Report the malaria status.
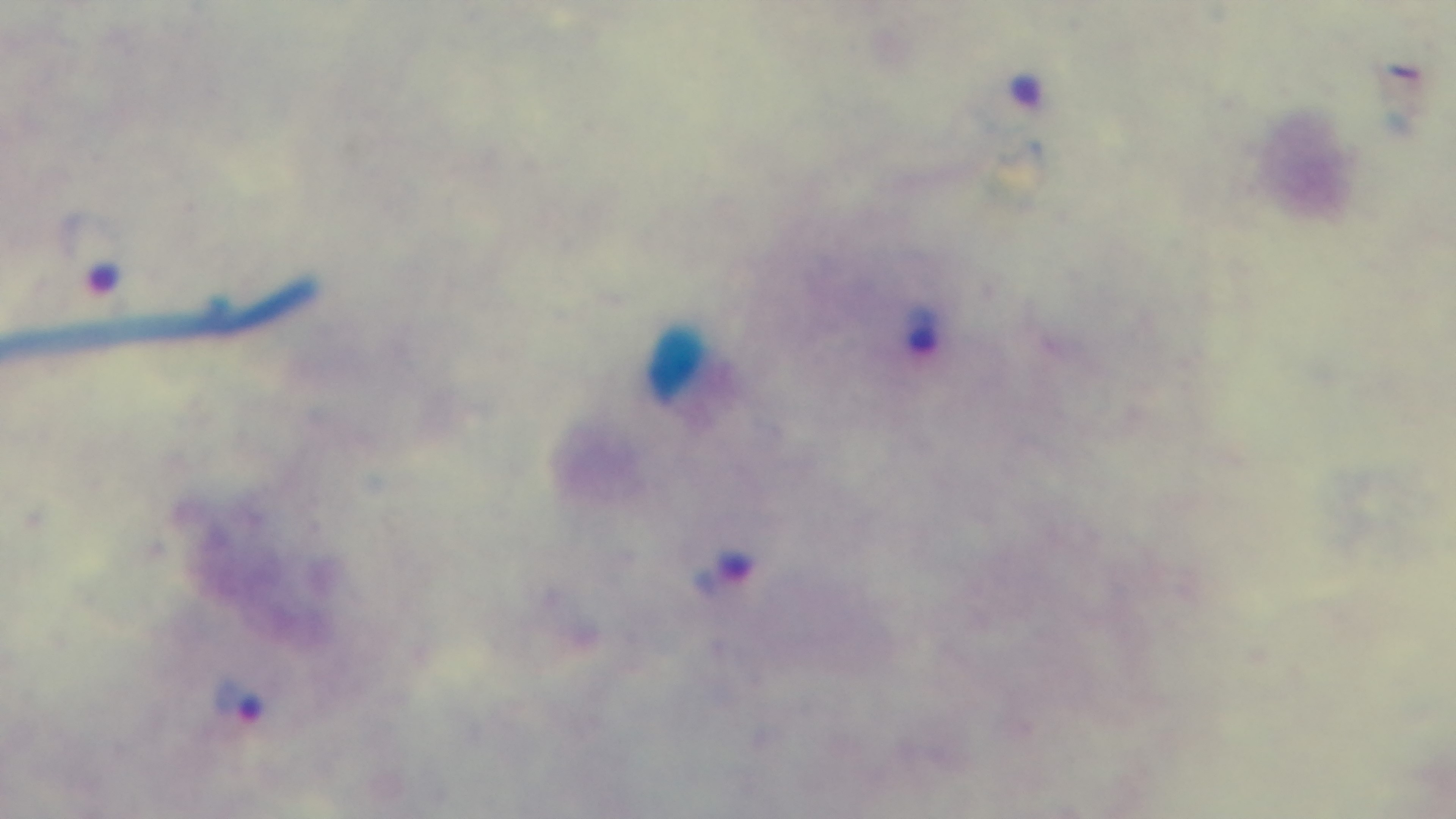

Infected.

modality = light microscopy
preparation = thick smear
stain = Giemsa
capture = mounted 4K digital camera
field of view = single
objective = 100x oil immersion